Assess this cell for malaria.
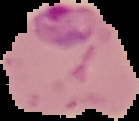

Parasitized.

Summary:
  - Image size: 139×121 pixels
  - Image type: segmented cell region with the area outside set to black
  - Preparation: thin blood smear